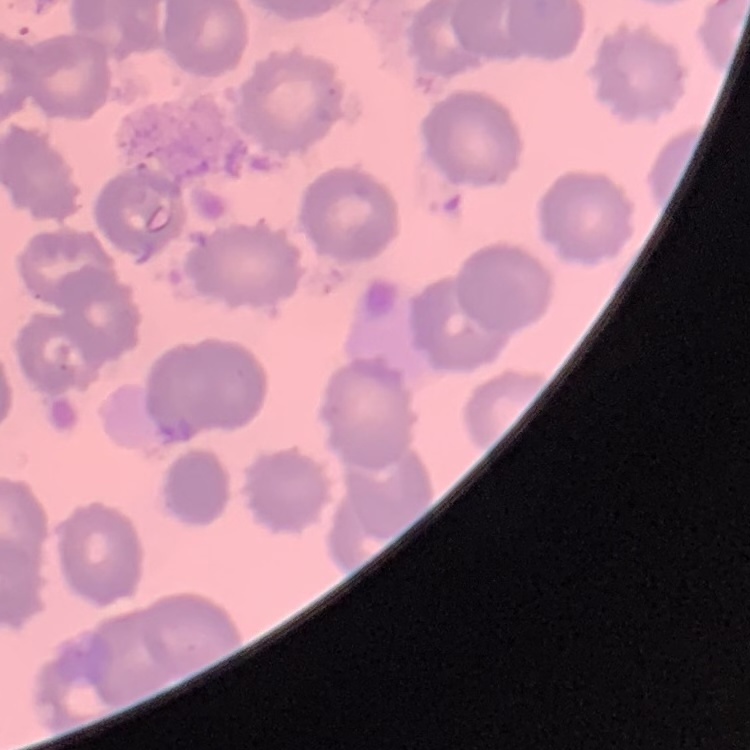
Summary:
  - Erythrocyte morphology: no rouleaux formation
  - Stain: Field's or Giemsa
  - Preparation: thin blood film
  - Image type: square crop of a larger photomicrograph